Identify the parasite.
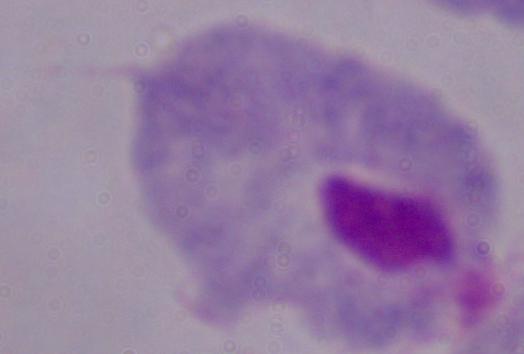
This is a trichomonad.

modality: micrograph
magnification: 1000x